Name the blood parasite species.
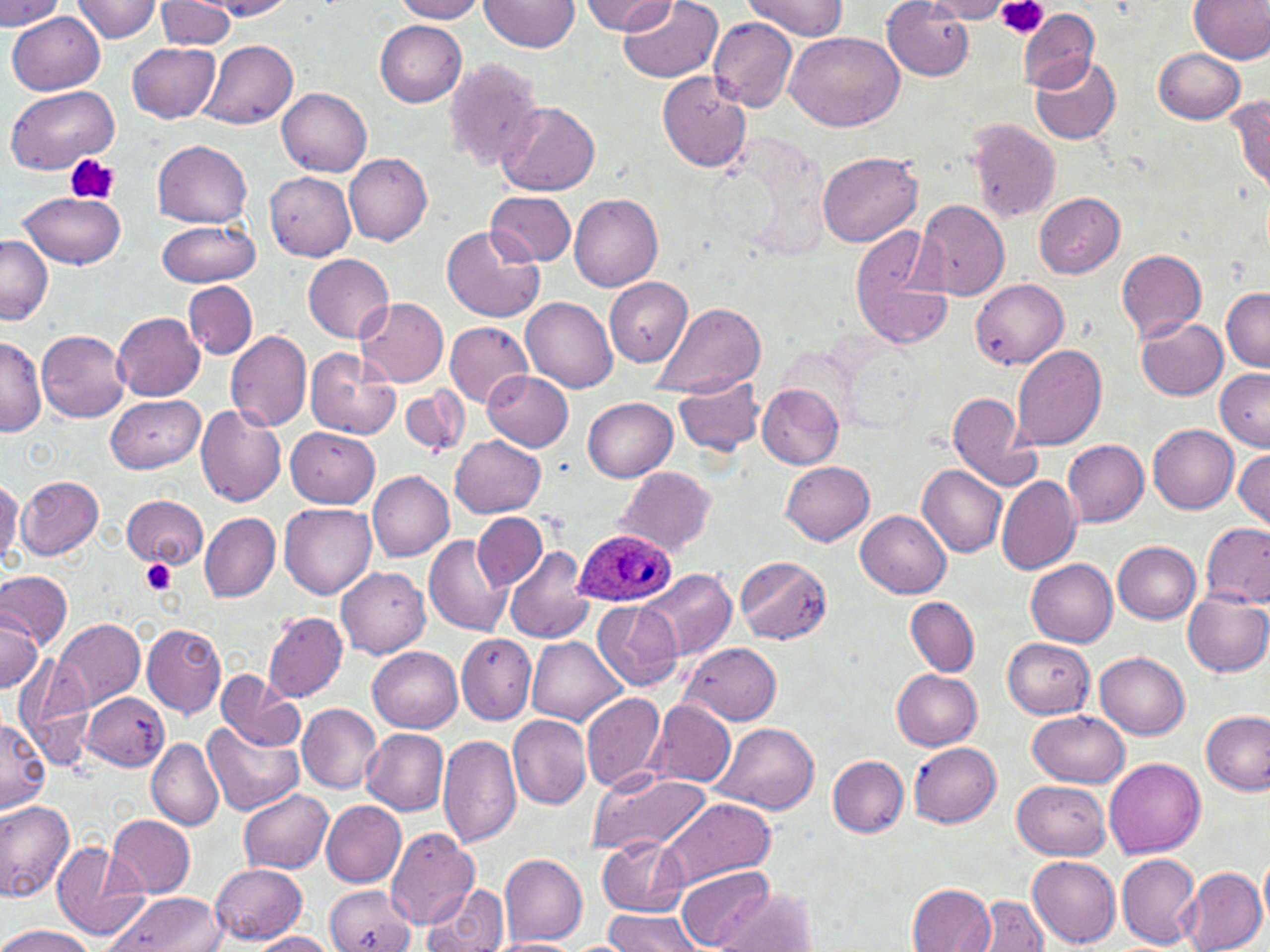
Plasmodium ovale.

magnification = 1000x
Plasmodium ovale-infected red blood cell locations = approximate bounding boxes as [x1, y1, x2, y2] in pixels: [574, 528, 677, 607]
platelet locations = approximate bounding boxes as [x1, y1, x2, y2] in pixels: [994, 0, 1048, 41], [66, 154, 117, 205], [140, 561, 177, 594]
field of view = single
stain = May-Grünwald-Giemsa
preparation = thin blood film
image size = 1270×952 pixels
modality = optical microscopy
uninfected red blood cell locations = approximate bounding boxes as [x1, y1, x2, y2] in pixels: [73, 0, 163, 42], [210, 0, 297, 20], [393, 0, 486, 21], [480, 0, 580, 53], [619, 0, 724, 83], [1188, 0, 1270, 63], [0, 1, 63, 30], [157, 1, 235, 50], [580, 1, 675, 33], [742, 1, 848, 39], [883, 1, 975, 80], [919, 1, 1015, 21], [1016, 9, 1100, 93], [7, 12, 106, 96], [707, 17, 798, 113], [375, 21, 467, 106], [784, 31, 905, 131], [199, 40, 298, 130], [127, 42, 220, 123], [1154, 48, 1245, 124], [1030, 54, 1122, 144], [443, 57, 543, 174], [656, 71, 752, 173], [4, 85, 120, 174], [278, 88, 371, 177], [1228, 91, 1270, 192], [495, 102, 600, 197], [965, 119, 1060, 223], [152, 140, 253, 227], [816, 150, 923, 248], [343, 153, 432, 244], [265, 172, 357, 261], [486, 189, 578, 266], [16, 191, 125, 268], [568, 191, 664, 292], [1035, 192, 1125, 277], [915, 198, 1010, 299], [156, 219, 260, 287], [443, 224, 545, 324], [850, 225, 953, 350], [1, 235, 53, 326], [1115, 249, 1208, 342], [304, 253, 394, 342], [604, 277, 694, 366], [971, 279, 1068, 368], [184, 282, 257, 360], [1221, 286, 1270, 370], [521, 297, 618, 392], [356, 298, 449, 388], [652, 303, 767, 399], [112, 312, 205, 401], [1136, 318, 1229, 401], [444, 322, 532, 407], [36, 329, 132, 424], [225, 331, 312, 433], [0, 335, 45, 438], [1010, 345, 1106, 450], [305, 350, 400, 439], [1215, 368, 1270, 450], [482, 369, 574, 450], [673, 375, 765, 458], [756, 382, 843, 469], [400, 386, 469, 457], [944, 390, 1040, 490], [105, 395, 204, 472], [584, 397, 677, 481], [194, 406, 288, 506], [1148, 425, 1239, 513], [286, 427, 380, 508], [451, 435, 546, 518], [1064, 439, 1149, 527], [1233, 448, 1269, 528], [780, 460, 875, 545], [918, 465, 1008, 559], [615, 468, 718, 556], [366, 470, 454, 560], [15, 474, 104, 559], [996, 475, 1081, 577], [0, 477, 24, 569], [120, 494, 210, 569], [280, 502, 376, 599], [855, 509, 951, 596], [201, 513, 279, 602], [472, 513, 547, 590], [1199, 520, 1270, 609], [424, 534, 512, 637], [1112, 542, 1201, 623], [504, 546, 593, 643], [733, 554, 834, 642], [1026, 559, 1117, 646], [337, 567, 431, 658], [641, 567, 736, 661], [0, 571, 72, 649], [1183, 589, 1270, 678], [906, 597, 978, 675], [593, 600, 682, 690], [0, 610, 41, 693], [263, 612, 348, 701], [54, 619, 145, 711], [142, 623, 227, 719], [457, 632, 537, 724], [527, 636, 625, 726], [1002, 637, 1095, 718], [682, 642, 781, 725], [369, 646, 463, 733], [1094, 652, 1191, 739], [14, 656, 96, 768], [215, 668, 306, 751], [892, 669, 981, 750], [81, 692, 170, 772], [580, 692, 667, 792], [645, 698, 736, 787], [297, 705, 382, 792], [1029, 710, 1129, 788], [1200, 711, 1268, 795], [509, 715, 591, 810], [0, 716, 49, 814], [202, 722, 303, 816], [712, 723, 820, 813], [363, 729, 450, 813], [437, 733, 522, 848], [147, 739, 224, 830], [909, 742, 1002, 828], [827, 755, 908, 837], [1104, 756, 1204, 856], [589, 768, 710, 857], [1012, 780, 1111, 861], [219, 790, 320, 939], [239, 790, 333, 875], [658, 796, 775, 888], [0, 799, 75, 901], [321, 801, 406, 886], [107, 814, 196, 897], [384, 828, 481, 930], [598, 835, 691, 915], [51, 844, 149, 942], [1115, 852, 1201, 949], [499, 853, 588, 945], [1028, 854, 1120, 948], [1259, 855, 1270, 930], [210, 862, 308, 943], [676, 866, 774, 950], [1178, 868, 1267, 952], [909, 882, 995, 951], [423, 883, 508, 952], [326, 884, 418, 952], [713, 888, 818, 952], [103, 892, 226, 951], [971, 895, 1051, 951], [604, 909, 704, 952], [0, 923, 94, 952], [243, 932, 341, 951], [490, 938, 589, 952]